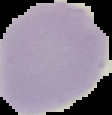
From a thin blood smear. Segmented cell region on a black background. Image is 112×115 pixels. Result: negative for Plasmodium parasites.